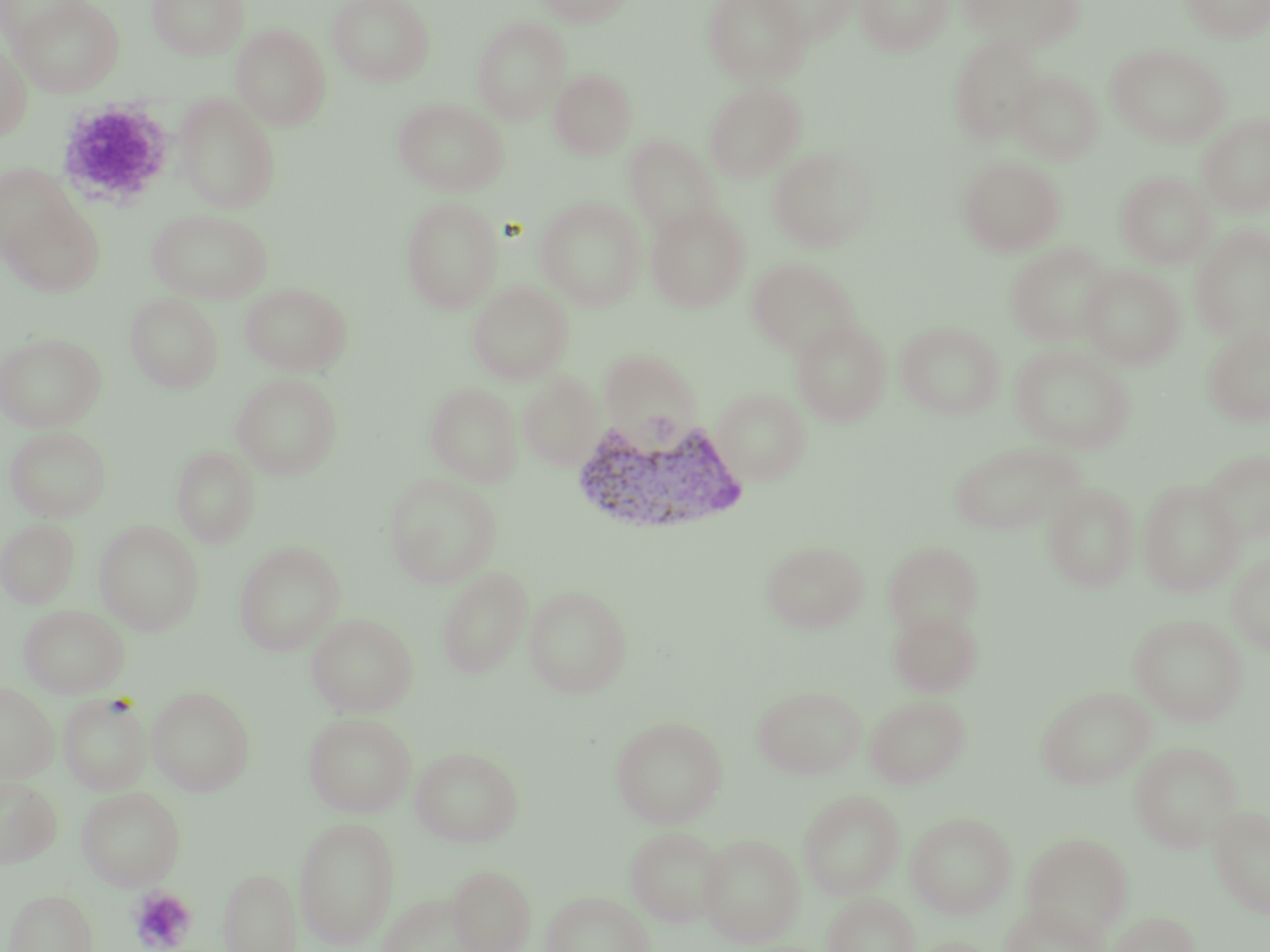

slide-level diagnosis = Plasmodium vivax
preparation = thin blood smear
modality = optical microscopy
image size = 1270×952 pixels
Plasmodium vivax-infected red blood cell locations = approximate bounding boxes as [x1, y1, x2, y2] in pixels: [567, 415, 750, 539]
platelet locations = approximate bounding boxes as [x1, y1, x2, y2] in pixels: [55, 99, 176, 210], [129, 886, 197, 952]
field of view = single
uninfected red blood cell locations = approximate bounding boxes as [x1, y1, x2, y2] in pixels: [0, 0, 93, 51], [11, 0, 124, 97], [147, 0, 249, 60], [327, 0, 434, 86], [535, 0, 631, 27], [703, 0, 810, 85], [756, 0, 860, 45], [856, 0, 953, 56], [958, 0, 1083, 46], [1180, 0, 1270, 42], [471, 17, 570, 124], [231, 24, 331, 131], [949, 34, 1045, 145], [0, 44, 32, 142], [1107, 44, 1230, 147], [549, 69, 637, 159], [1009, 70, 1103, 164], [704, 82, 806, 182], [174, 93, 281, 214], [393, 99, 507, 195], [1198, 113, 1270, 217], [623, 135, 722, 239], [767, 147, 877, 251], [958, 156, 1065, 256], [0, 164, 78, 262], [1115, 171, 1215, 269], [1, 193, 105, 297], [401, 196, 502, 314], [536, 196, 646, 311], [645, 204, 750, 313], [147, 209, 273, 303], [1190, 226, 1270, 342], [1005, 242, 1115, 347], [747, 257, 859, 356], [1079, 265, 1185, 369], [468, 280, 573, 385], [239, 282, 352, 376], [767, 284, 883, 396], [125, 293, 223, 393], [791, 318, 892, 426], [895, 322, 1005, 419], [1202, 325, 1270, 427], [0, 332, 106, 432], [1010, 345, 1135, 453], [599, 348, 701, 443], [518, 372, 604, 470], [231, 373, 342, 480], [426, 382, 522, 486], [713, 387, 811, 484], [4, 426, 111, 522], [949, 441, 1084, 536], [172, 445, 260, 547], [1200, 449, 1270, 544], [383, 473, 502, 588], [1138, 480, 1244, 596], [1042, 483, 1139, 592], [1, 518, 79, 608], [94, 520, 204, 636], [761, 540, 869, 633], [883, 541, 983, 636], [233, 542, 345, 655], [1227, 553, 1270, 654], [437, 565, 533, 680], [524, 584, 633, 698], [18, 604, 129, 698], [887, 608, 982, 698], [306, 613, 417, 717], [1129, 614, 1248, 726], [0, 680, 59, 783], [147, 686, 255, 796], [753, 686, 866, 780], [1036, 687, 1156, 789], [58, 693, 152, 796], [865, 696, 968, 788], [303, 712, 416, 817], [610, 715, 728, 828], [1129, 741, 1242, 852], [411, 746, 523, 847], [0, 776, 61, 868], [76, 786, 185, 890], [798, 789, 904, 900], [1208, 804, 1270, 918], [906, 812, 1016, 919], [293, 816, 400, 949], [625, 826, 725, 927], [1022, 832, 1133, 939], [698, 833, 804, 947], [448, 864, 536, 952], [218, 868, 301, 952], [3, 889, 99, 952], [541, 891, 655, 952], [377, 893, 486, 951], [823, 893, 919, 952], [1000, 902, 1106, 952], [1106, 911, 1200, 952], [907, 938, 1003, 952]
magnification = 1000x
stain = May-Grünwald-Giemsa